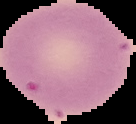
Summary:
  - Malaria status: uninfected
  - Image type: segmented cell region with the area outside set to black
  - Image size: 136×124 pixels
  - Preparation: thin blood smear